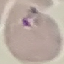
Summary:
  - Malaria status: parasitized
  - Stain: Giemsa
  - Capture: smartphone through the microscope eyepiece
  - Preparation: thin smear
  - Image type: automatically extracted cell patch, resized to 64 × 64 pixels